State which parasite is depicted.
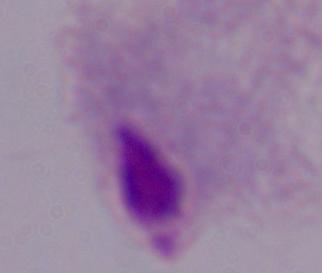
This is a trichomonad.

modality = photomicrograph
magnification = 1000x